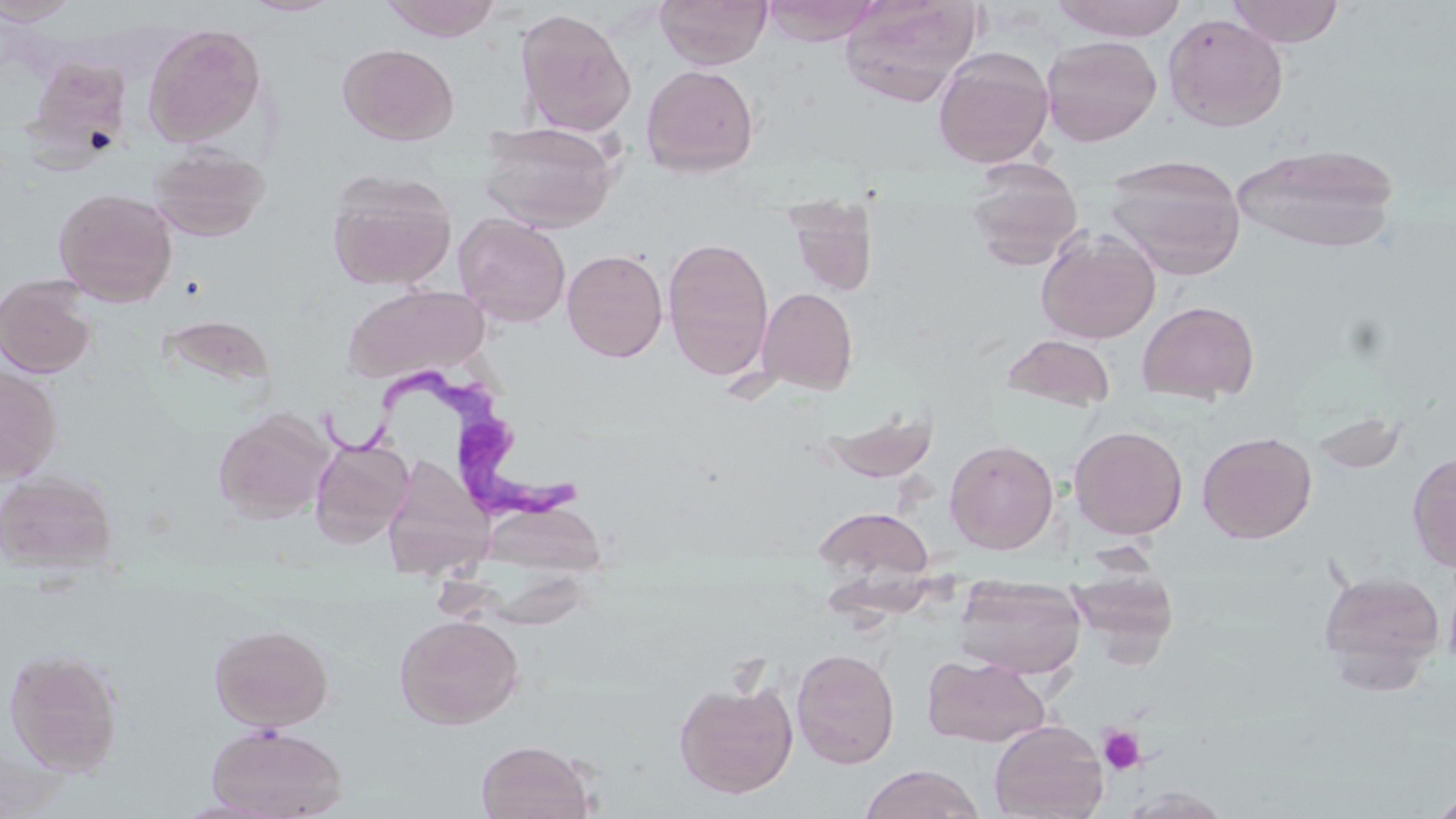

Approximate bounding boxes as (x1, y1, x2, y2) in pixels. Platelet locations: (1098, 724, 1146, 775). Trypanosoma brucei locations: (332, 358, 593, 534). Uninfected red blood cell locations: (0, 0, 81, 25), (239, 0, 346, 17), (380, 0, 502, 41), (655, 0, 773, 69), (760, 0, 884, 46), (839, 0, 982, 106), (1049, 0, 1189, 41), (1225, 0, 1347, 47), (514, 8, 637, 136), (1163, 13, 1289, 132), (143, 23, 266, 147), (1042, 35, 1163, 147), (337, 43, 459, 145), (932, 46, 1054, 168), (24, 56, 133, 161), (641, 64, 759, 177), (478, 121, 620, 232), (1233, 142, 1401, 254), (147, 145, 271, 242), (1105, 154, 1246, 280), (964, 158, 1084, 269), (327, 169, 456, 290), (53, 187, 178, 307), (787, 201, 877, 295), (454, 212, 571, 327), (1036, 227, 1161, 344), (661, 236, 775, 381), (562, 249, 668, 362), (0, 274, 98, 379), (341, 284, 492, 383), (757, 286, 858, 394), (1137, 300, 1260, 404), (156, 313, 277, 398), (1002, 334, 1116, 412), (0, 366, 63, 482), (817, 403, 940, 484), (213, 408, 335, 524), (1308, 411, 1410, 477), (1070, 425, 1188, 539), (1197, 431, 1317, 543), (310, 438, 413, 547), (945, 438, 1059, 554), (1407, 451, 1456, 572), (391, 456, 493, 612), (0, 470, 119, 574), (482, 500, 608, 580), (812, 506, 935, 587), (1441, 551, 1456, 677), (1069, 564, 1179, 662), (1318, 568, 1445, 685), (954, 576, 1086, 680), (393, 613, 524, 729), (208, 622, 335, 731), (3, 646, 124, 776), (791, 648, 900, 768), (923, 655, 1049, 747), (674, 679, 798, 799), (989, 719, 1108, 819), (204, 724, 350, 819), (475, 739, 597, 819), (858, 764, 986, 819), (1119, 787, 1233, 819), (1426, 788, 1456, 818). Slide-level diagnosis: Trypanosoma brucei. Image is 1456×819 pixels. Captured at 1000x magnification. Optical microscopy. Thin blood film. Single field of view. May-Grünwald-Giemsa stain.